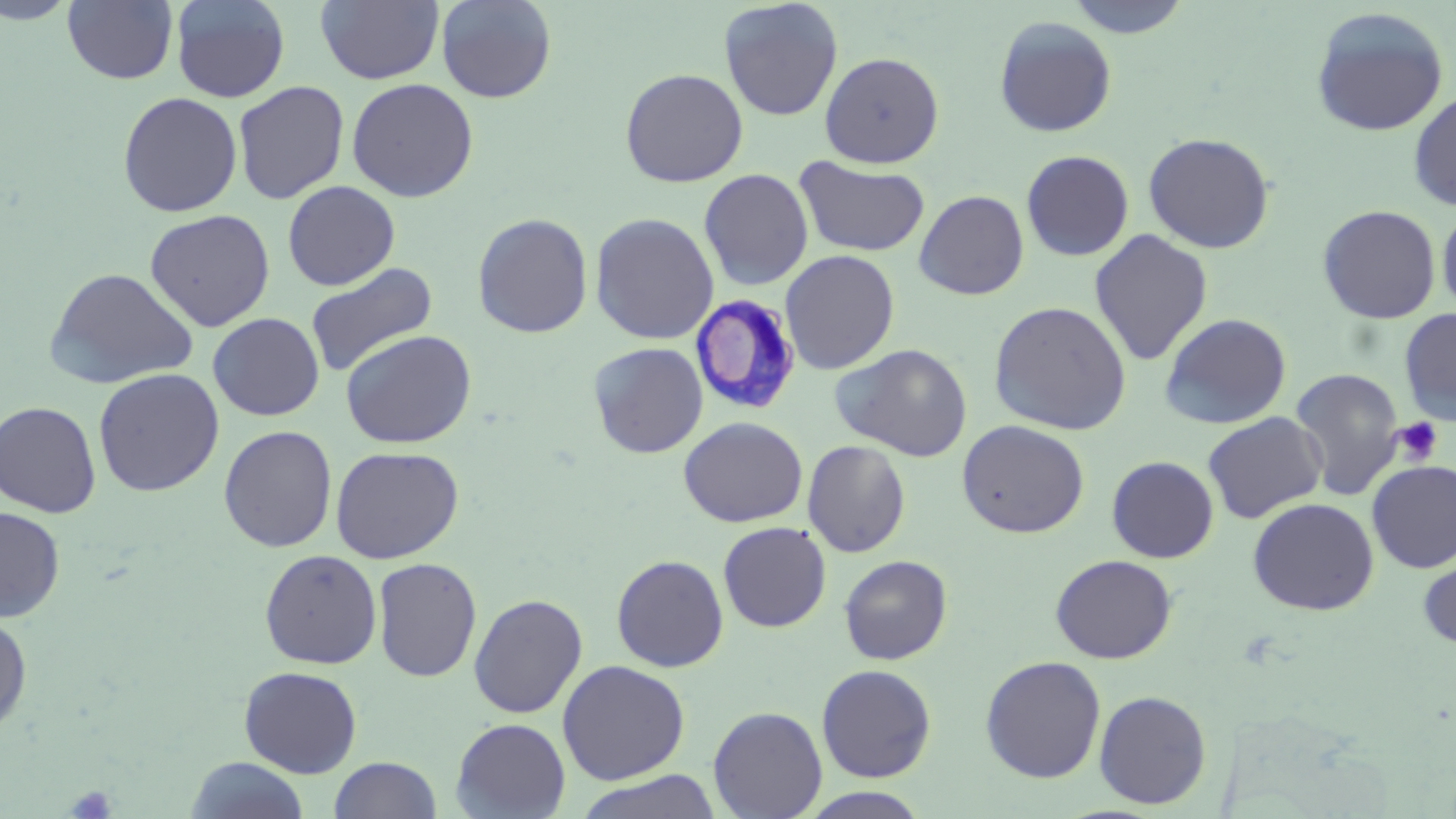 Approximate bounding boxes as (x1,y1)-(x2,y2) corner pairs in pixels. Trypanosoma brucei locations: (689,294)-(802,415). Uninfected red blood cell locations: (63,0)-(178,84), (171,0)-(290,103), (316,0)-(444,85), (435,0)-(558,104), (718,0)-(843,121), (1064,0)-(1193,38), (0,1)-(80,25), (1310,7)-(1450,137), (993,15)-(1117,137), (819,50)-(945,168), (619,67)-(748,187), (346,78)-(479,203), (233,81)-(349,204), (1408,91)-(1456,211), (117,92)-(242,217), (1143,132)-(1275,253), (1021,150)-(1134,261), (794,157)-(930,257), (698,168)-(814,291), (283,180)-(400,290), (914,190)-(1029,300), (1317,204)-(1441,324), (1437,204)-(1456,317), (144,209)-(275,331), (472,212)-(594,338), (589,212)-(720,345), (1089,230)-(1213,366), (780,249)-(900,375), (305,262)-(438,379), (43,267)-(199,390), (988,301)-(1132,435), (1398,307)-(1456,426), (1159,312)-(1292,430), (208,313)-(324,421), (341,329)-(477,449), (588,341)-(708,458), (832,343)-(972,462), (93,368)-(225,497), (1290,368)-(1405,501), (0,401)-(101,518), (1202,411)-(1328,524), (679,416)-(807,527), (956,419)-(1090,538), (218,425)-(338,552), (802,440)-(911,558), (330,446)-(464,563), (1106,455)-(1219,563), (1367,461)-(1456,573), (1247,497)-(1379,615), (0,506)-(65,623), (717,521)-(831,633), (259,549)-(382,669), (1417,549)-(1456,651), (611,554)-(729,672), (839,554)-(952,665), (1050,554)-(1176,664), (372,557)-(482,683), (468,593)-(588,718), (0,613)-(33,738), (980,655)-(1106,783), (556,659)-(690,785), (816,663)-(937,782), (239,666)-(363,778), (1094,689)-(1212,810), (708,706)-(828,819), (451,718)-(571,819), (186,756)-(309,818), (328,756)-(442,818), (572,771)-(724,819), (799,787)-(933,818). Platelet locations: (1392,418)-(1443,465), (67,784)-(116,818). Slide-level diagnosis: Trypanosoma brucei. Single field of view. Captured at 1000x magnification. Thin blood film. Image is 1456×819 pixels. May-Grünwald-Giemsa-stained preparation. Optical microscopy.